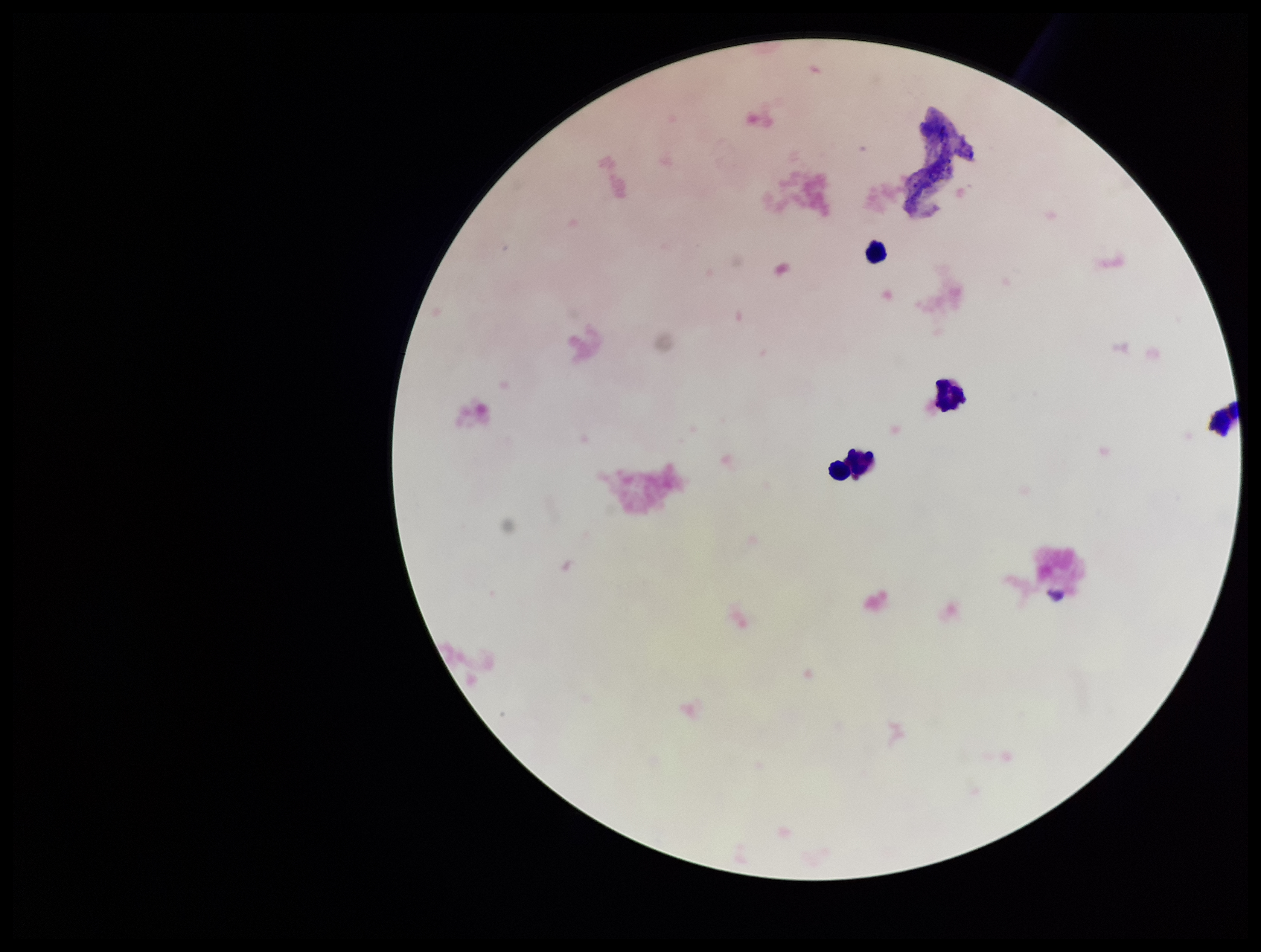

{
  "field_of_view": "one from this slide",
  "capture": "smartphone photograph through the microscope eyepiece",
  "stain": "Giemsa",
  "leukocyte_count": 3,
  "preparation": "thick blood smear",
  "image_size": "1261×952 pixels",
  "parasite_count": 0,
  "plasmodium_parasites": "none identified",
  "patient_malaria_status": "negative"
}